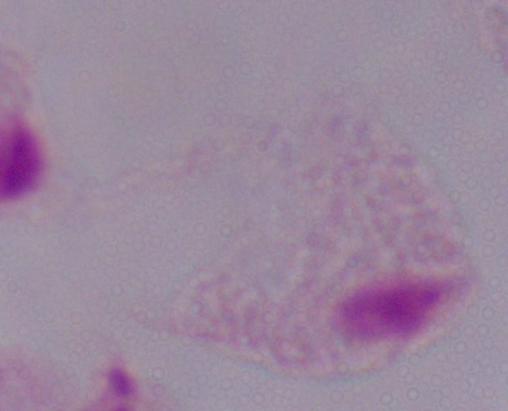
identification = trichomonad
magnification = 1000x
modality = photomicrograph